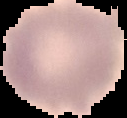
Summary:
  - Image size: 127×118 pixels
  - Result: negative for Plasmodium parasites
  - Image type: segmented cell region on a black background
  - Preparation: thin blood smear